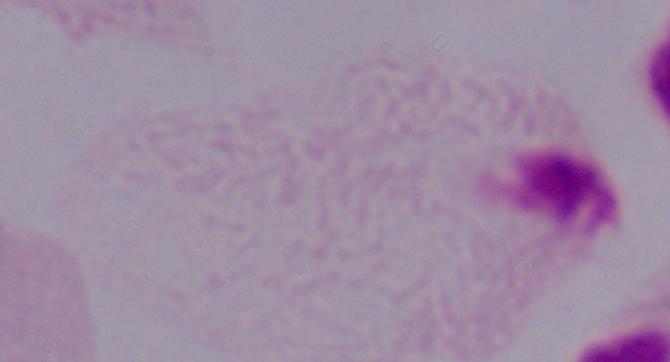

A trichomonad is seen. Captured at 1000x magnification. Photomicrograph.